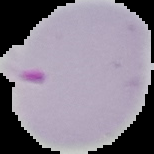

image size = 154×154 pixels
preparation = thin blood smear
malaria status = parasitized
image type = segmented cell region on a black background